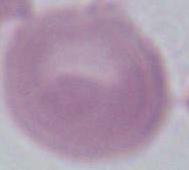

Summary:
  - Magnification: 1000x
  - Modality: micrograph
  - Identification: erythrocyte